Report the malaria status of this cell.
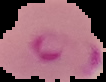

Parasitized.

Summary:
  - Image type: cell region segmented out of the field of view; surrounding area masked to black
  - Image size: 106×82 pixels
  - Preparation: thin blood smear